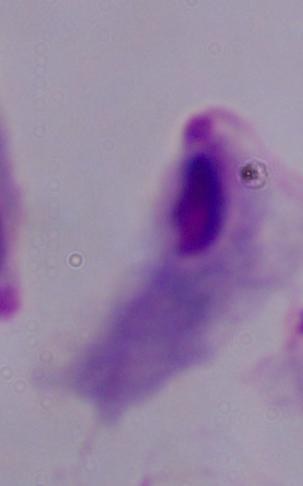

identification = trichomonad
magnification = 1000x
modality = photomicrograph